Assess this cell for malaria.
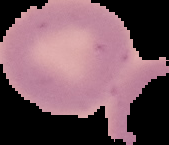
Uninfected.

Summary:
  - Image type: cell region segmented out of the field of view; surrounding area masked to black
  - Image size: 169×145 pixels
  - Preparation: thin blood film